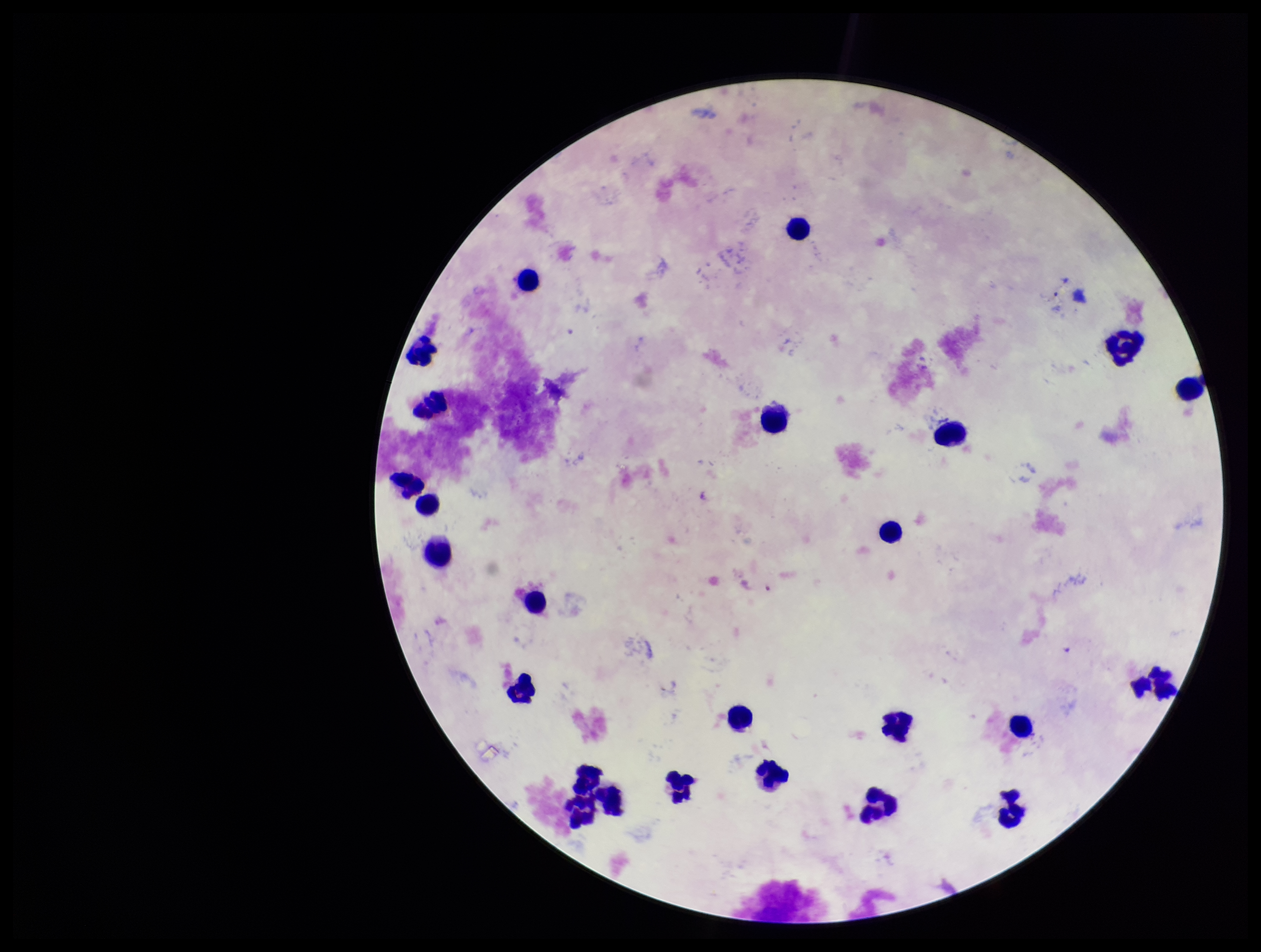

Summary:
  - Image size: 1261×952 pixels
  - Parasite count: 0
  - Stain: Giemsa
  - Patient malaria status: negative
  - Capture: smartphone photograph through the microscope eyepiece
  - Leukocyte count: 25
  - Plasmodium parasites: none seen
  - Field of view: one from this slide
  - Preparation: thick